Report the malaria status of this cell.
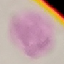
It is uninfected.

Giemsa-stained preparation. Thin smear of blood. Automatically extracted cell patch, resized to 64 × 64 pixels. Acquired by smartphone through the microscope eyepiece.